Outline each P. falciparum parasite and classify it by life-cycle stage.
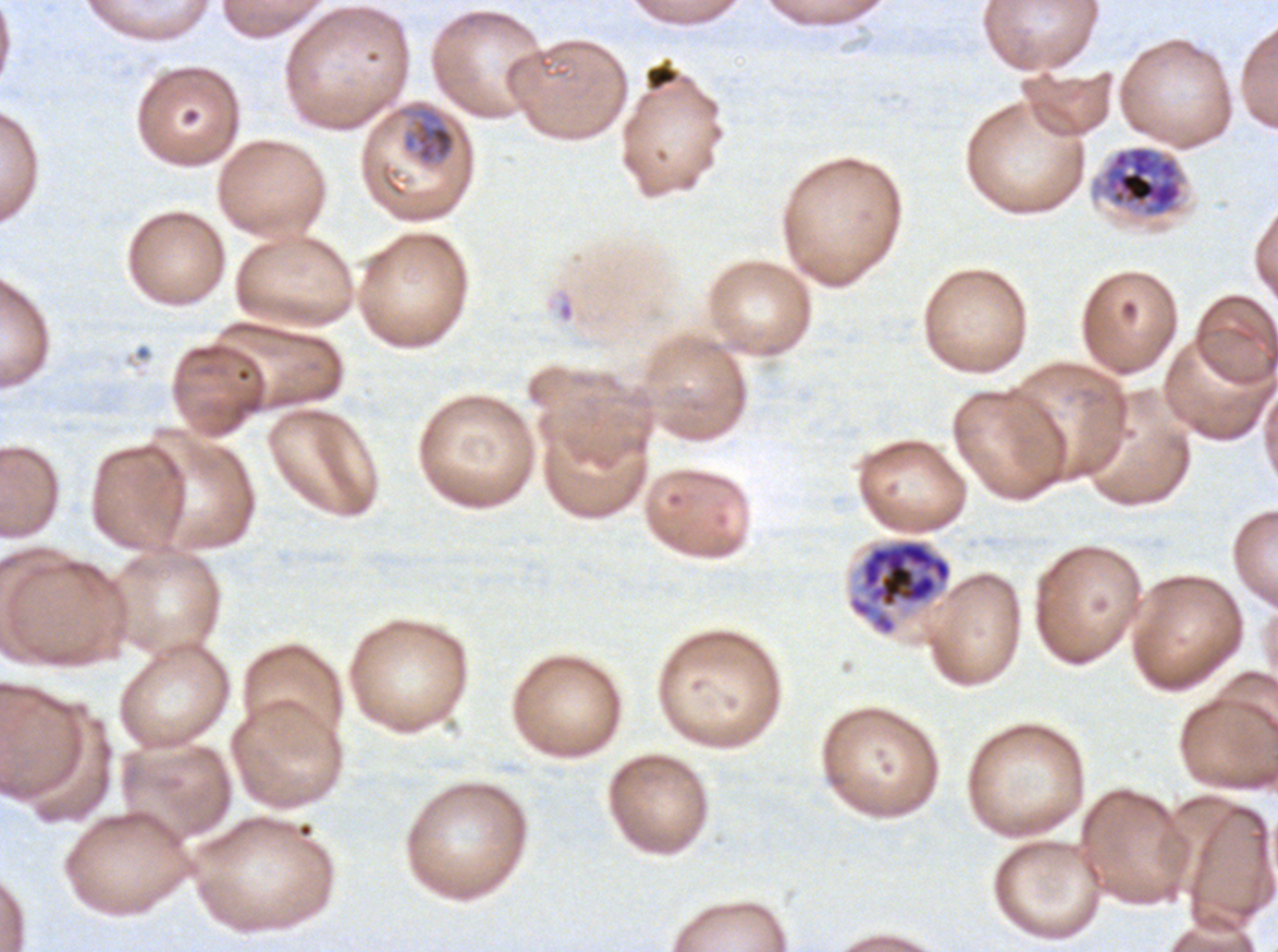
Approximate bounding boxes as {x1, y1, x2, y2} in pixels.
Mid trophozoites: {397, 105, 458, 167}.
Late schizonts: {1100, 145, 1184, 217}.
Segmenters: {847, 538, 953, 637}.
No rings, late-ring/early-trophozoite forms, late trophozoites, early schizonts, or gametocytes observed.

{
  "preparation": "thin blood smear",
  "life_cycle_stages_observed": "mid trophozoite, late schizont, segmenter",
  "debris_locations": "approximate bounding boxes as {x1, y1, x2, y2} in pixels: {644, 57, 680, 92}",
  "field_of_view": "one sub-image of a larger composite",
  "stain": "Giemsa",
  "image_size": "1278×952 pixels",
  "specimen": "P. falciparum from a patient in The Gambia, cultured ex vivo for 24 to 48 hours"
}